Point out leukocytes.
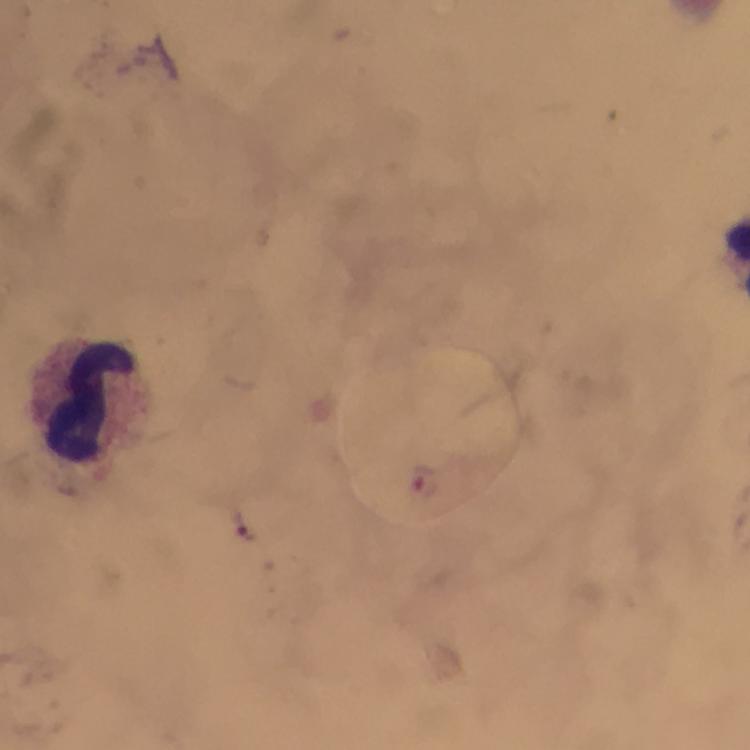

Approximate object centers, in pixels from the top-left corner.
Leukocytes: (x=88, y=402).

Malaria parasites: none detected. A crop from one field of view. Image is 750×750 pixels. At 100x magnification. Photographed with a smartphone mounted on the microscope. Immersion oil was used. Thick smear. Giemsa stain. From a malaria diagnostic workup.